Report the malaria status of this cell.
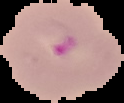

Parasitized.

From a thin blood film. Image is 124×103 pixels. The area outside the segmented cell region is set to black.